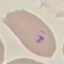

Summary:
  - Result: malaria parasites detected
  - Stain: Giemsa
  - Capture: smartphone through the microscope eyepiece
  - Preparation: thin smear
  - Image type: automatically extracted cell patch, resized to 64 × 64 pixels